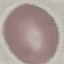

malaria status = uninfected
image type = cell patch, automatically extracted from a larger field of view and resized to 64 × 64 pixels
preparation = thin smear
stain = Giemsa
capture = smartphone through the microscope eyepiece